Locate every Babesia divergens-infected red blood cell.
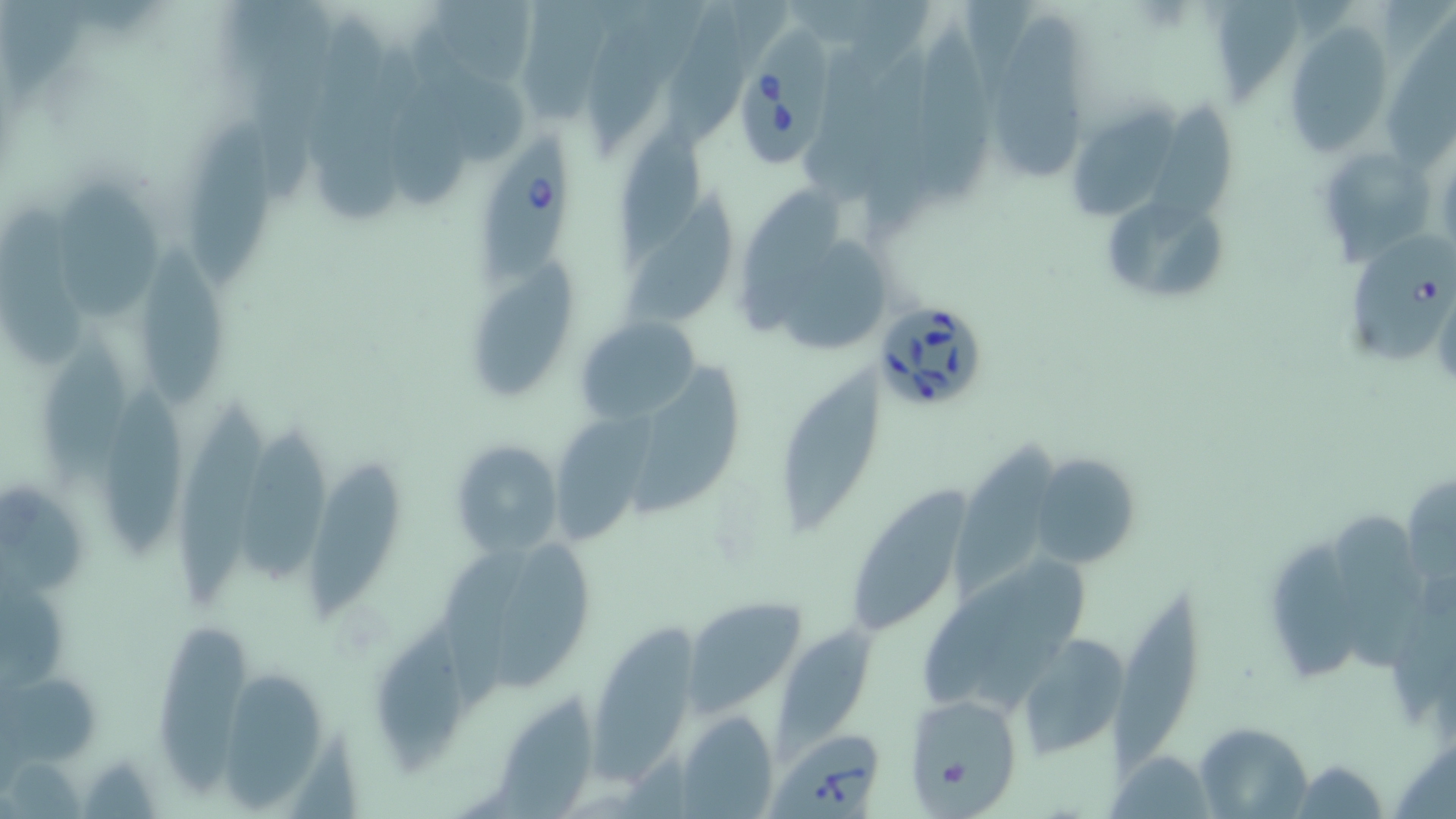

Approximate bounding boxes as named x1/y1/x2/y2 corners in pixels.
Babesia divergens-infected red blood cells: (x1=722, y1=28, x2=842, y2=169), (x1=479, y1=131, x2=574, y2=286), (x1=1349, y1=237, x2=1455, y2=366), (x1=867, y1=296, x2=991, y2=413), (x1=772, y1=730, x2=886, y2=818).

slide_level_diagnosis: Babesia divergens
magnification: 1000x
modality: light microscopy
image_size: 1456×819 pixels
field_of_view: single
stain: May-Grünwald-Giemsa
uninfected_red_blood_cell_locations: 'approximate bounding boxes as named x1/y1/x2/y2 corners in pixels: (x1=588, y1=1, x2=706, y2=151), (x1=992, y1=17, x2=1091, y2=178), (x1=912, y1=21, x2=1000, y2=208), (x1=1380, y1=24, x2=1455, y2=176), (x1=1285, y1=25, x2=1396, y2=156), (x1=414, y1=31, x2=532, y2=168), (x1=324, y1=53, x2=413, y2=220), (x1=1074, y1=96, x2=1181, y2=218), (x1=1145, y1=104, x2=1235, y2=239), (x1=192, y1=122, x2=277, y2=286), (x1=614, y1=122, x2=711, y2=261), (x1=1327, y1=146, x2=1440, y2=260), (x1=739, y1=176, x2=851, y2=338), (x1=59, y1=183, x2=164, y2=322), (x1=627, y1=186, x2=736, y2=327), (x1=0, y1=202, x2=95, y2=366), (x1=1106, y1=209, x2=1231, y2=296), (x1=788, y1=238, x2=896, y2=350), (x1=139, y1=248, x2=227, y2=409), (x1=471, y1=259, x2=582, y2=399), (x1=575, y1=315, x2=702, y2=424), (x1=43, y1=328, x2=134, y2=489), (x1=780, y1=358, x2=878, y2=538), (x1=627, y1=359, x2=739, y2=530), (x1=106, y1=381, x2=188, y2=566), (x1=548, y1=401, x2=661, y2=539), (x1=168, y1=402, x2=269, y2=611), (x1=236, y1=425, x2=331, y2=590), (x1=952, y1=437, x2=1066, y2=599), (x1=448, y1=439, x2=562, y2=559), (x1=1029, y1=452, x2=1140, y2=569), (x1=303, y1=462, x2=399, y2=626), (x1=854, y1=480, x2=973, y2=641), (x1=0, y1=482, x2=95, y2=603), (x1=1332, y1=500, x2=1426, y2=673), (x1=1268, y1=535, x2=1357, y2=697), (x1=438, y1=538, x2=540, y2=719), (x1=495, y1=542, x2=599, y2=692), (x1=1109, y1=590, x2=1207, y2=779), (x1=687, y1=599, x2=807, y2=716), (x1=589, y1=618, x2=705, y2=795), (x1=374, y1=621, x2=469, y2=772), (x1=153, y1=623, x2=251, y2=802), (x1=776, y1=626, x2=879, y2=755), (x1=1019, y1=634, x2=1130, y2=759), (x1=222, y1=670, x2=331, y2=814), (x1=5, y1=672, x2=100, y2=765), (x1=495, y1=690, x2=599, y2=819), (x1=902, y1=691, x2=1026, y2=810), (x1=680, y1=710, x2=777, y2=818), (x1=1194, y1=723, x2=1311, y2=816), (x1=1114, y1=749, x2=1211, y2=818), (x1=1294, y1=762, x2=1386, y2=816)'
preparation: thin blood smear